Report the malaria status of this cell.
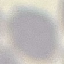

It is uninfected.

image_type: automatically extracted cell patch, resized to 64 × 64 pixels
stain: Giemsa
capture: smartphone camera at the microscope eyepiece
preparation: thin smear